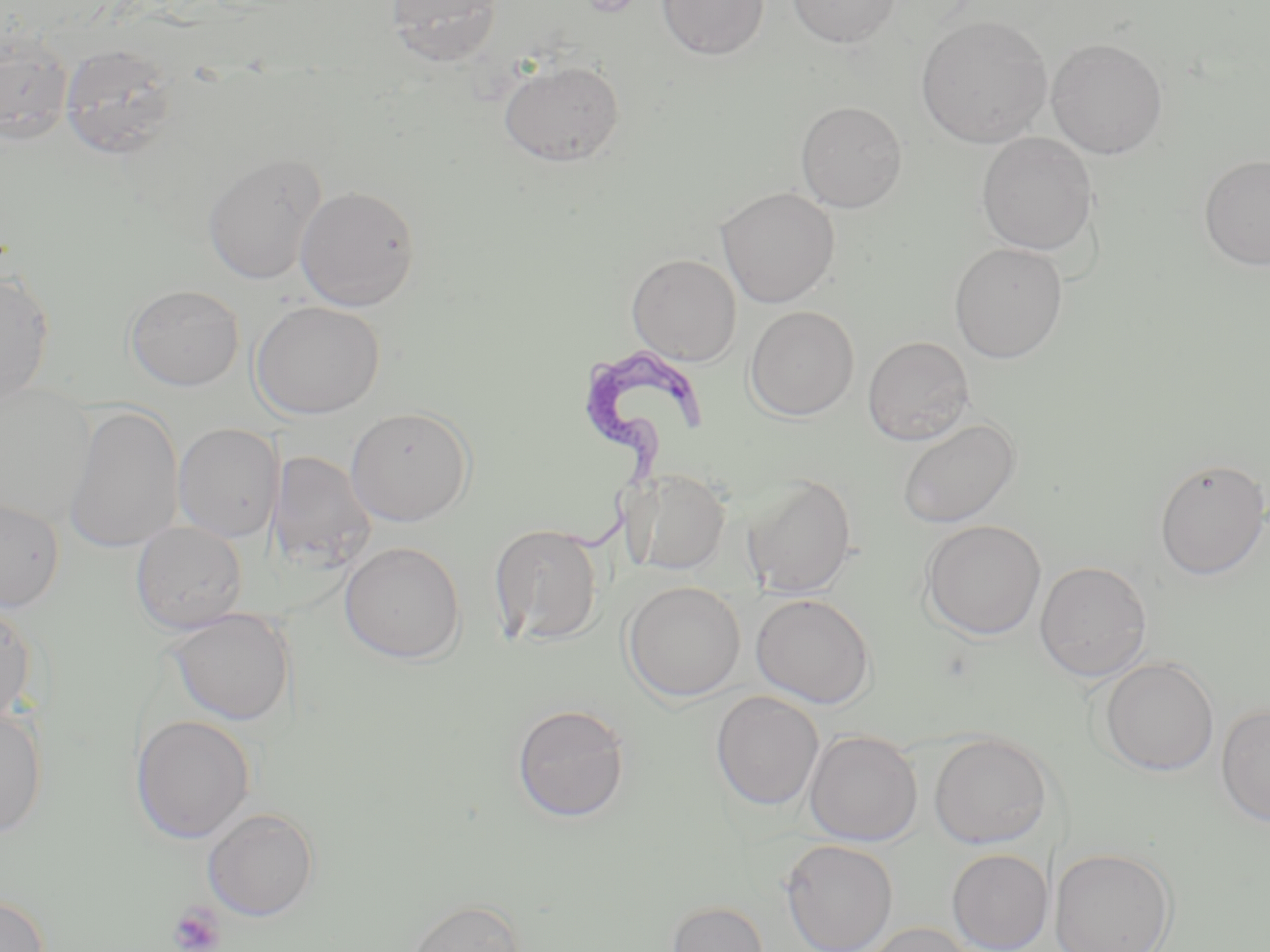
Summary:
  - Coordinate format: approximate bounding boxes as (x1,y1)-(x2,y2) corner pairs in pixels
  - Uninfected red blood cell locations: (385,0)-(506,66), (657,0)-(770,61), (787,0)-(900,47), (916,15)-(1052,148), (1,32)-(74,145), (1046,37)-(1168,159), (59,43)-(179,159), (499,60)-(624,167), (796,100)-(907,213), (976,132)-(1098,256), (203,153)-(327,286), (1199,153)-(1270,272), (295,185)-(421,311), (717,187)-(840,308), (949,242)-(1068,364), (626,253)-(741,366), (0,271)-(55,405), (125,283)-(244,391), (250,301)-(386,419), (745,305)-(859,421), (862,336)-(974,445), (1,382)-(97,526), (63,404)-(185,552), (346,406)-(475,526), (897,418)-(1021,528), (173,423)-(284,542), (268,451)-(375,573), (1153,458)-(1270,580), (625,469)-(731,576), (742,474)-(857,598), (0,496)-(65,611), (921,520)-(1046,639), (131,521)-(248,634), (489,523)-(604,646), (339,541)-(466,664), (1035,561)-(1152,682), (623,581)-(745,701), (751,593)-(876,708), (0,601)-(38,725), (167,608)-(295,726), (1098,657)-(1219,776), (711,691)-(824,810), (512,703)-(631,822), (1216,703)-(1270,828), (0,706)-(48,838), (130,714)-(256,844), (804,729)-(923,846), (929,731)-(1053,849), (202,806)-(320,921), (780,838)-(898,952), (1050,846)-(1177,952), (947,848)-(1053,952), (0,891)-(50,952), (406,898)-(525,952), (666,900)-(769,952), (859,923)-(977,951)
  - Trypanosoma brucei locations: (557,344)-(707,551)
  - Platelet locations: (168,900)-(226,952)
  - Slide-level diagnosis: Trypanosoma brucei
  - Preparation: thin blood film
  - Field of view: single
  - Modality: optical microscopy
  - Stain: May-Grünwald-Giemsa
  - Magnification: 1000x
  - Image size: 1270×952 pixels